State which parasite is depicted.
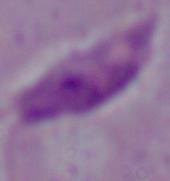
Leishmania.

magnification = 1000x
modality = photomicrograph